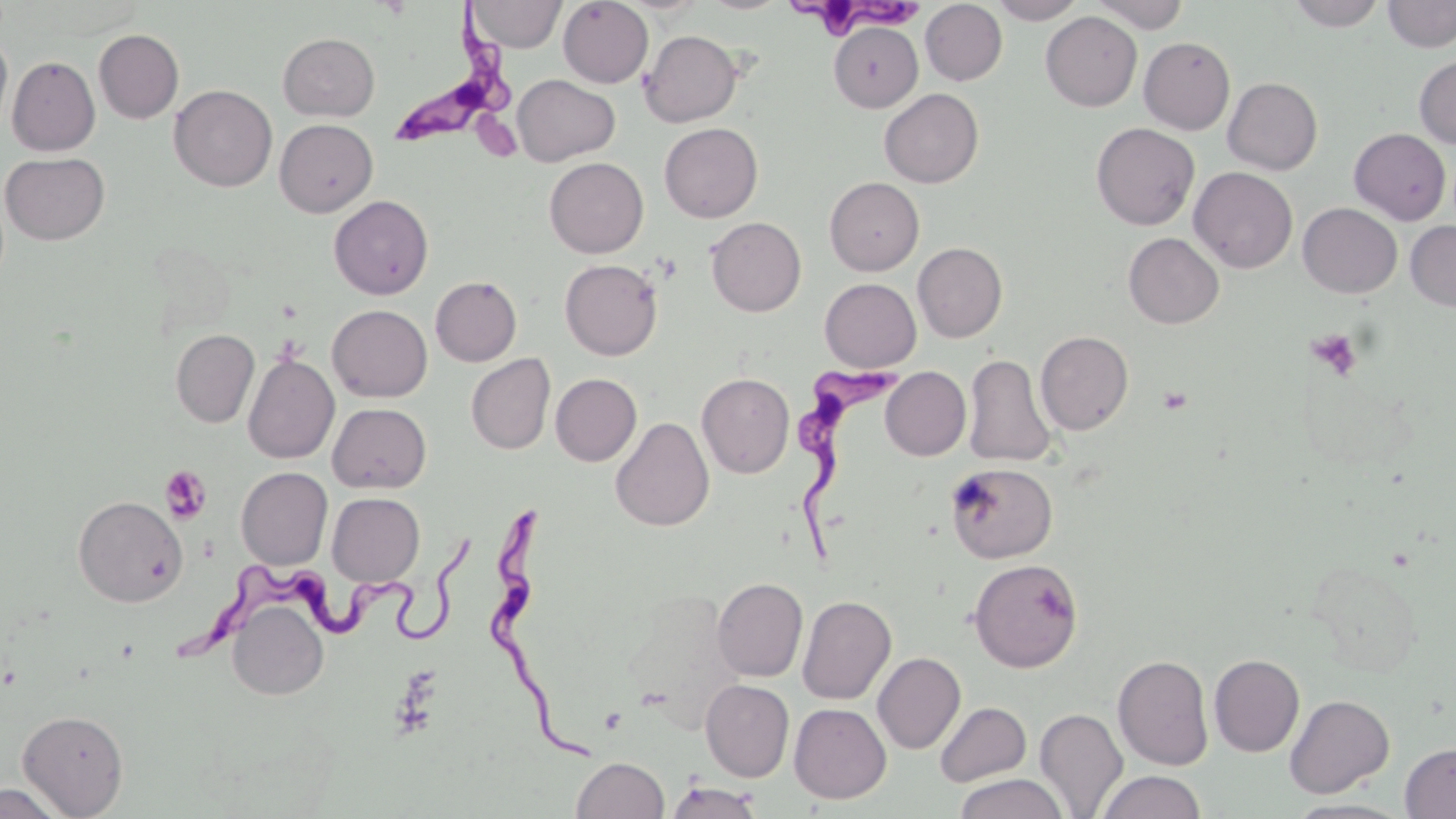
Approximate bounding boxes as [x1, y1, x2, y2] in pixels. Uninfected red blood cell locations: [469, 0, 566, 52], [558, 0, 653, 88], [700, 0, 789, 14], [989, 0, 1086, 24], [1089, 0, 1189, 33], [1288, 0, 1386, 31], [1384, 0, 1456, 52], [920, 1, 1007, 85], [1041, 11, 1142, 111], [829, 22, 923, 111], [93, 29, 183, 123], [640, 30, 742, 127], [0, 32, 13, 137], [278, 32, 380, 121], [1139, 37, 1235, 134], [1414, 55, 1456, 149], [7, 56, 100, 156], [512, 75, 620, 166], [1223, 77, 1323, 175], [169, 84, 278, 192], [879, 88, 983, 188], [274, 118, 378, 217], [659, 122, 763, 222], [1091, 123, 1200, 230], [1349, 128, 1451, 224], [1, 152, 110, 245], [544, 157, 649, 258], [1188, 166, 1297, 273], [825, 177, 924, 276], [329, 195, 433, 299], [1298, 203, 1402, 298], [706, 217, 806, 317], [1405, 220, 1456, 312], [1123, 232, 1224, 328], [913, 242, 1007, 342], [560, 259, 663, 360], [430, 276, 522, 366], [819, 278, 921, 372], [327, 304, 432, 402], [170, 329, 259, 428], [1035, 330, 1134, 435], [243, 352, 339, 464], [465, 353, 556, 455], [964, 354, 1056, 467], [881, 367, 971, 461], [696, 372, 794, 478], [550, 373, 641, 465], [328, 403, 431, 494], [610, 416, 715, 531], [945, 463, 1057, 563], [236, 466, 333, 569], [327, 492, 424, 586], [72, 495, 188, 607], [968, 558, 1083, 672], [1307, 559, 1423, 677], [712, 578, 808, 682], [621, 589, 745, 734], [797, 595, 896, 705], [228, 599, 329, 701], [873, 652, 966, 754], [1112, 654, 1214, 770], [1209, 654, 1304, 756], [700, 679, 794, 782], [1285, 694, 1395, 797], [935, 702, 1031, 787], [789, 703, 891, 803], [1034, 707, 1128, 818], [18, 709, 128, 817], [1400, 742, 1456, 818], [570, 756, 670, 819], [1096, 770, 1206, 819], [954, 773, 1067, 819], [665, 781, 765, 819], [0, 783, 69, 819], [1283, 798, 1413, 819]. Trypanosoma brucei locations: [787, 0, 929, 42], [379, 1, 517, 152], [795, 356, 914, 566], [480, 498, 597, 759], [177, 525, 477, 667]. Platelet locations: [1307, 329, 1362, 380], [1157, 385, 1193, 415], [159, 465, 213, 524]. Slide-level diagnosis: Trypanosoma brucei. Optical microscopy. Image is 1456×819 pixels. Thin blood smear. May-Grünwald-Giemsa stain. One field of a larger specimen. Captured at 1000x magnification.